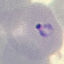 Malaria status: parasitized. Thin smear of blood. Photographed with a smartphone camera at the microscope eyepiece. Automatically extracted cell patch, resized to 64 × 64 pixels. Giemsa stain.